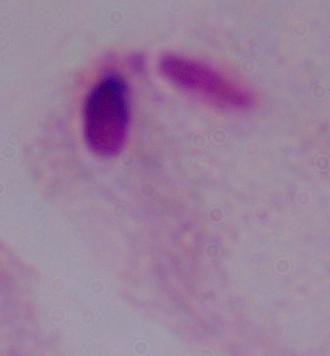

Summary:
  - Magnification: 1000x
  - Modality: photomicrograph
  - Identification: trichomonad